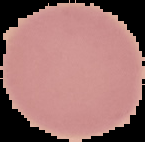
Image is 145×142 pixels. From a thin blood smear. Segmented cell region on a black background. Malaria status: uninfected.